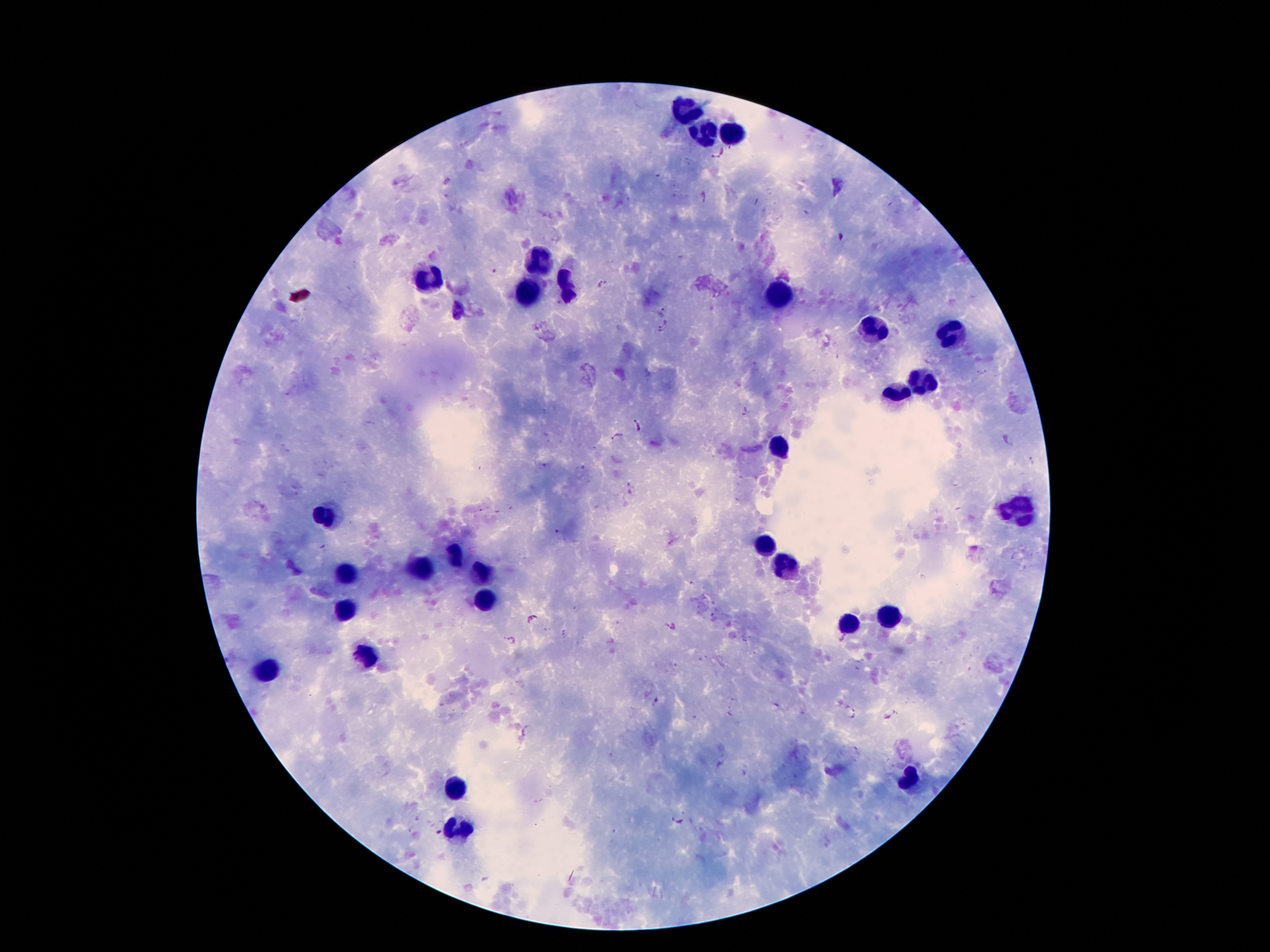 Approximate centers as [x, y] in pixels. Malaria parasite locations: [720, 153], [704, 197], [842, 236], [603, 282], [662, 311], [663, 326], [635, 425], [616, 435], [532, 619], [663, 625], [676, 628], [509, 639], [852, 712], [889, 714], [525, 729], [677, 819]. Leukocyte locations: [687, 113], [703, 131], [730, 131], [539, 260], [426, 283], [570, 289], [529, 291], [777, 295], [873, 332], [947, 334], [924, 381], [894, 391], [781, 449], [1019, 510], [324, 512], [765, 541], [453, 555], [420, 565], [783, 567], [344, 572], [484, 576], [486, 598], [344, 613], [890, 617], [849, 625], [369, 654], [266, 670], [908, 778], [459, 789], [459, 834]. Image is 1270×952 pixels. Smartphone photograph taken through the microscope eyepiece. 100x magnification. Giemsa stain. One field from this slide. Thick blood film. Patient malaria status: positive for Plasmodium falciparum.